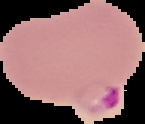
Result: Plasmodium parasites detected. From a thin blood film. Segmented cell region on a black background. Image is 145×124 pixels.